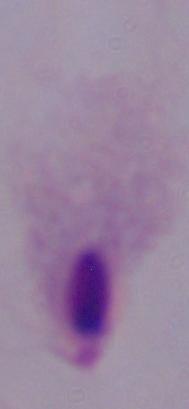
{
  "modality": "micrograph",
  "identification": "trichomonad",
  "magnification": "1000x"
}